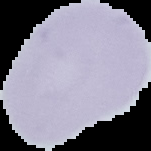

Malaria status: uninfected. From a thin blood film. Cell region segmented out of the field of view; the surrounding area is masked to black. Image is 151×151 pixels.